Assess this cell for malaria.
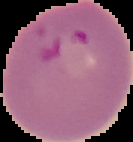

It is parasitized.

Image is 133×142 pixels. The area outside the segmented cell region is set to black. From a thin blood film.